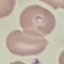

Malaria status: parasitized. Thin smear of blood. Acquired by smartphone through the microscope eyepiece. Cell patch, automatically extracted from a larger field of view and resized to 64 × 64 pixels. Giemsa stain.